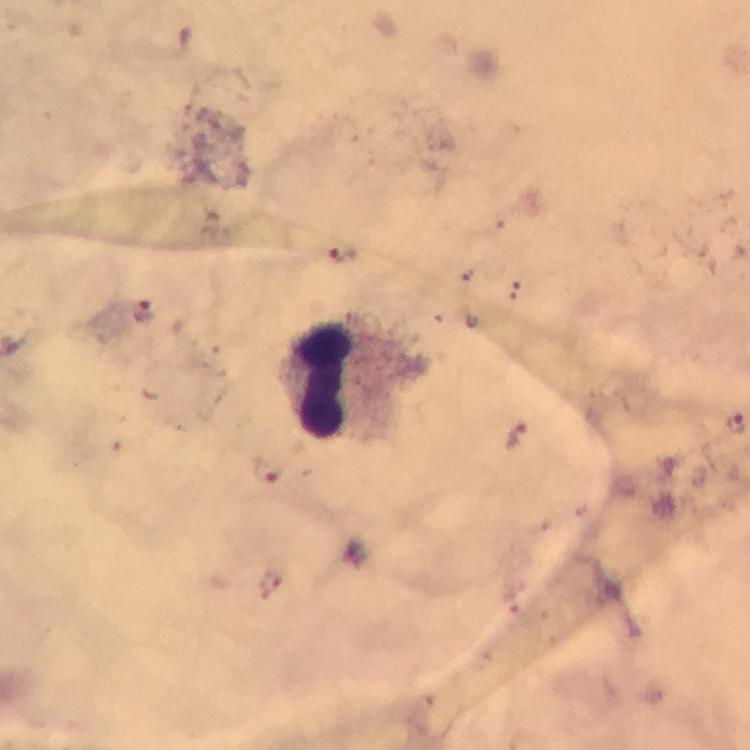

magnification = 100x
immersion oil = applied
leukocyte locations = approximate object centers, in pixels from the top-left corner: (x=324, y=376)
image size = 750×750 pixels
Plasmodium parasite locations = approximate object centers, in pixels from the top-left corner: (x=343, y=254), (x=143, y=309), (x=734, y=423), (x=514, y=434), (x=270, y=467)
preparation = thick blood film
stain = Giemsa
capture = smartphone mounted on the microscope
context = from a malaria diagnostic workup
cropped from = one field of view